Locate and identify every blood parasite.
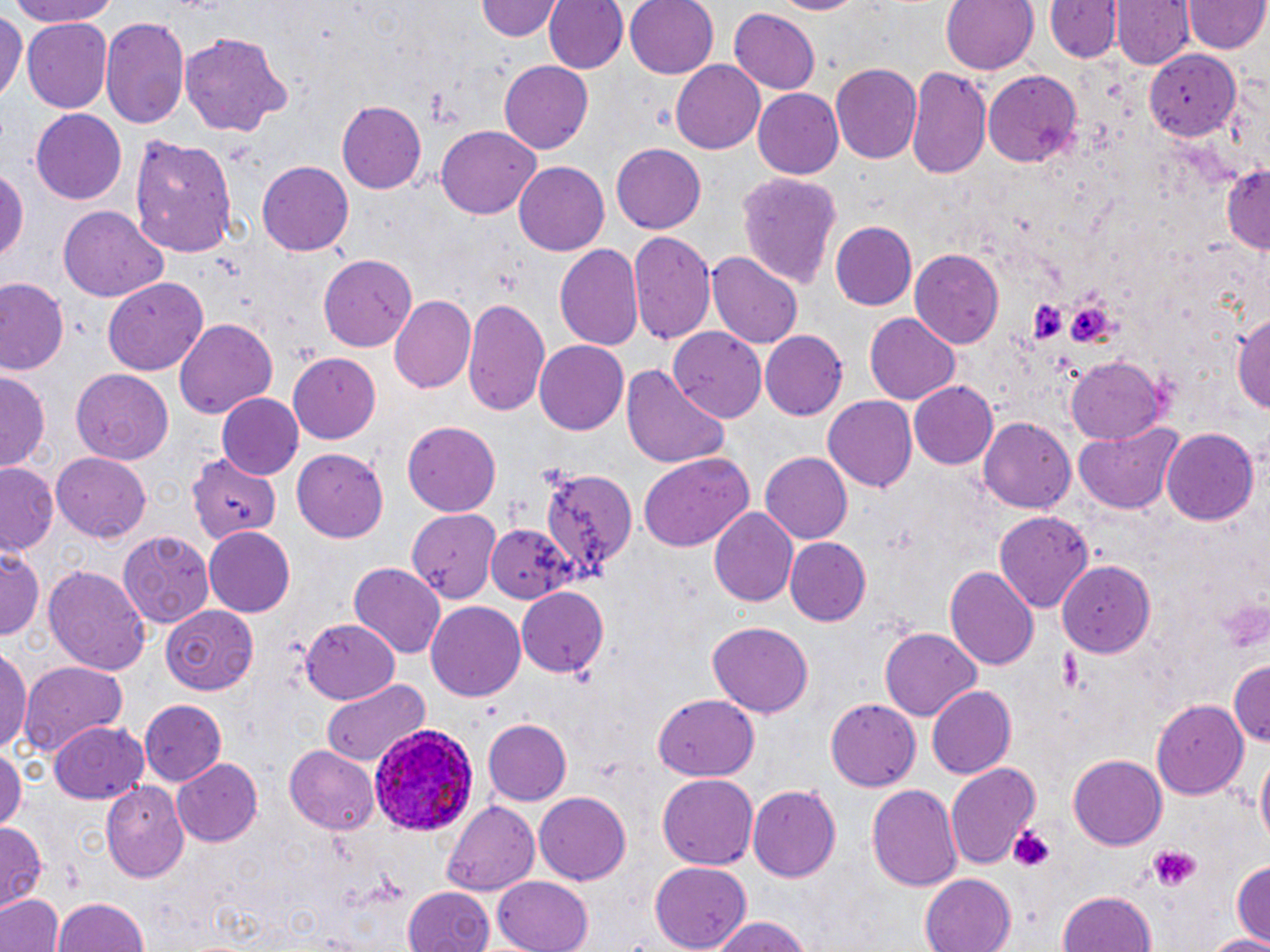
Approximate bounding boxes as [x1, y1, x2, y2] in pixels.
Plasmodium ovale-infected red blood cells: [368, 722, 480, 836].
No Plasmodium falciparum, Plasmodium malariae, Plasmodium vivax, Babesia divergens, or Trypanosoma brucei observed.

slide-level diagnosis = Plasmodium ovale
modality = optical microscopy
field of view = single
image size = 1270×952 pixels
stain = May-Grünwald-Giemsa
platelet locations = approximate bounding boxes as [x1, y1, x2, y2] in pixels: [1025, 297, 1070, 343], [1065, 298, 1117, 354], [1216, 595, 1267, 653], [1055, 646, 1093, 692], [1008, 824, 1059, 873], [1144, 843, 1200, 891]
magnification = 1000x
uninfected red blood cell locations = approximate bounding boxes as [x1, y1, x2, y2] in pixels: [1, 0, 122, 27], [477, 0, 563, 40], [543, 0, 627, 75], [625, 0, 720, 79], [771, 0, 865, 16], [941, 0, 1040, 76], [1045, 1, 1121, 64], [1113, 1, 1192, 69], [1186, 2, 1267, 55], [729, 7, 819, 94], [0, 9, 24, 106], [100, 14, 189, 127], [23, 20, 113, 112], [178, 32, 293, 137], [1145, 52, 1240, 138], [498, 60, 594, 155], [671, 60, 766, 154], [830, 62, 923, 164], [906, 68, 991, 183], [983, 69, 1084, 170], [753, 88, 845, 180], [335, 100, 426, 194], [30, 109, 128, 204], [435, 124, 541, 220], [127, 131, 241, 257], [611, 142, 705, 231], [257, 160, 354, 256], [514, 161, 609, 255], [1220, 161, 1269, 254], [0, 162, 28, 274], [736, 173, 843, 293], [58, 208, 169, 301], [830, 221, 917, 310], [630, 232, 716, 348], [554, 244, 645, 354], [911, 248, 1003, 347], [707, 251, 803, 350], [319, 255, 418, 352], [102, 277, 211, 375], [2, 281, 68, 376], [390, 295, 476, 395], [461, 297, 550, 416], [1232, 306, 1270, 417], [864, 313, 961, 404], [174, 317, 279, 419], [669, 329, 768, 423], [758, 330, 846, 421], [533, 339, 627, 436], [288, 353, 383, 444], [1065, 355, 1168, 444], [620, 365, 730, 470], [69, 368, 173, 464], [0, 371, 48, 471], [909, 382, 1000, 470], [216, 394, 303, 481], [823, 397, 917, 493], [980, 417, 1076, 511], [402, 419, 502, 516], [1075, 423, 1181, 514], [1162, 428, 1259, 526], [292, 449, 389, 542], [638, 451, 755, 553], [759, 451, 852, 544], [51, 452, 152, 542], [186, 454, 279, 542], [2, 463, 61, 556], [538, 469, 633, 580], [709, 505, 798, 606], [406, 510, 497, 601], [995, 511, 1095, 613], [486, 522, 577, 601], [202, 526, 295, 614], [119, 528, 213, 630], [787, 537, 872, 624], [0, 548, 43, 643], [1059, 559, 1156, 659], [41, 561, 153, 676], [349, 562, 446, 656], [945, 565, 1039, 671], [515, 586, 608, 676], [426, 602, 527, 701], [164, 606, 259, 695], [300, 619, 401, 703], [707, 620, 815, 717], [879, 627, 981, 719], [0, 647, 30, 759], [1228, 660, 1270, 751], [19, 661, 129, 755], [319, 678, 431, 767], [926, 685, 1018, 779], [653, 692, 761, 781], [821, 697, 918, 788], [139, 699, 226, 785], [1150, 701, 1247, 800], [482, 718, 573, 804], [50, 719, 150, 803], [0, 746, 23, 835], [284, 746, 381, 836], [1254, 751, 1269, 857], [1069, 754, 1167, 851], [171, 758, 263, 848], [946, 763, 1041, 871], [657, 773, 756, 871], [102, 782, 191, 880], [866, 782, 963, 894], [748, 783, 840, 882], [534, 792, 629, 884], [442, 798, 542, 895], [0, 822, 45, 909], [1230, 856, 1270, 947], [648, 862, 752, 951], [491, 875, 594, 952], [919, 875, 1017, 952], [1053, 887, 1159, 952], [402, 888, 497, 952], [0, 893, 63, 952], [53, 896, 152, 952], [707, 915, 818, 952], [1202, 932, 1270, 952]
preparation = thin blood film